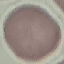

Summary:
  - Malaria status: uninfected
  - Capture: smartphone camera at the microscope eyepiece
  - Image type: automatically extracted cell patch, resized to 64 × 64 pixels
  - Preparation: thin blood film
  - Stain: Giemsa